Assess this cell for malaria.
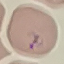

Uninfected.

stain: Giemsa
preparation: thin smear
image_type: cell patch, automatically extracted from a larger field of view and resized to 64 × 64 pixels
capture: smartphone camera at the microscope eyepiece